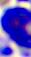
modality: micrograph
identification: leukocyte
magnification: 400x